Classify this cell by malaria status.
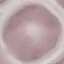
Uninfected.

Summary:
  - Image type: automatically extracted cell patch, resized to 64 × 64 pixels
  - Stain: Giemsa
  - Capture: smartphone camera at the microscope eyepiece
  - Preparation: thin smear